Identify the parasite.
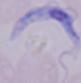
A trypanosome.

{
  "magnification": "1000x",
  "modality": "photomicrograph"
}